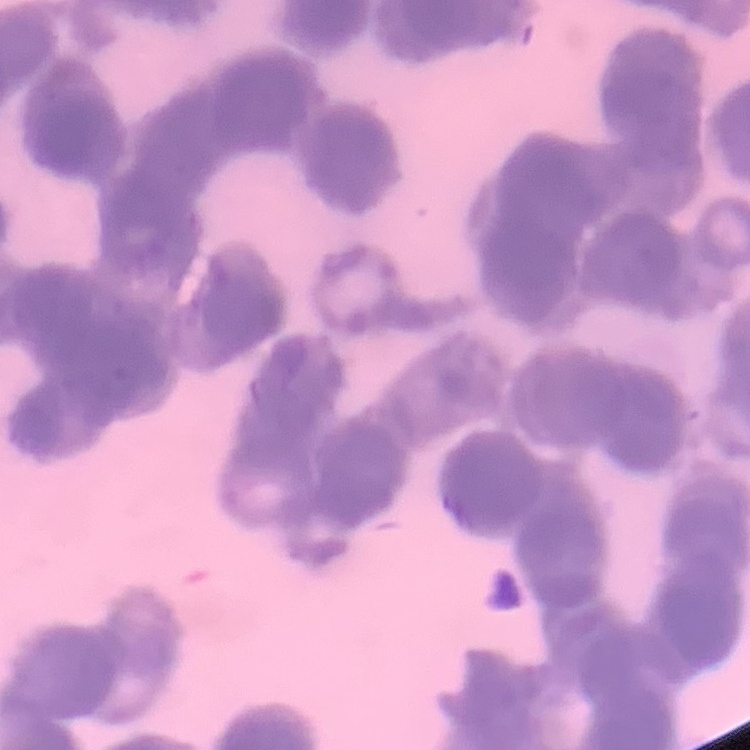 The red blood cells exhibit rouleaux formation. Stained with either Field's or Giemsa. One tile cut from a larger photomicrograph. Thin blood smear.